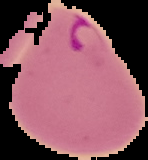
image_type: segmented cell region on a black background
malaria_status: parasitized
preparation: thin blood film
image_size: 148×160 pixels